Describe the morphology of the erythrocytes.
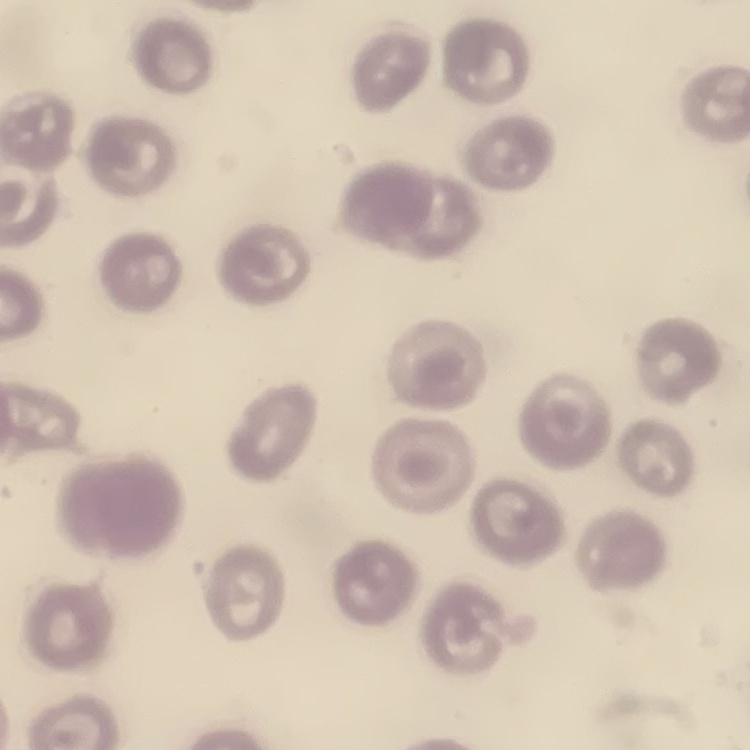

They show no rouleaux formation.

Summary:
  - Image type: square crop of a larger photomicrograph
  - Stain: Field's or Giemsa
  - Preparation: thin peripheral smear